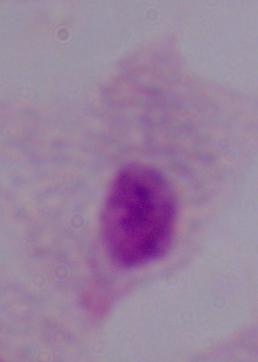

Summary:
  - Identification: trichomonad
  - Magnification: 1000x
  - Modality: photomicrograph